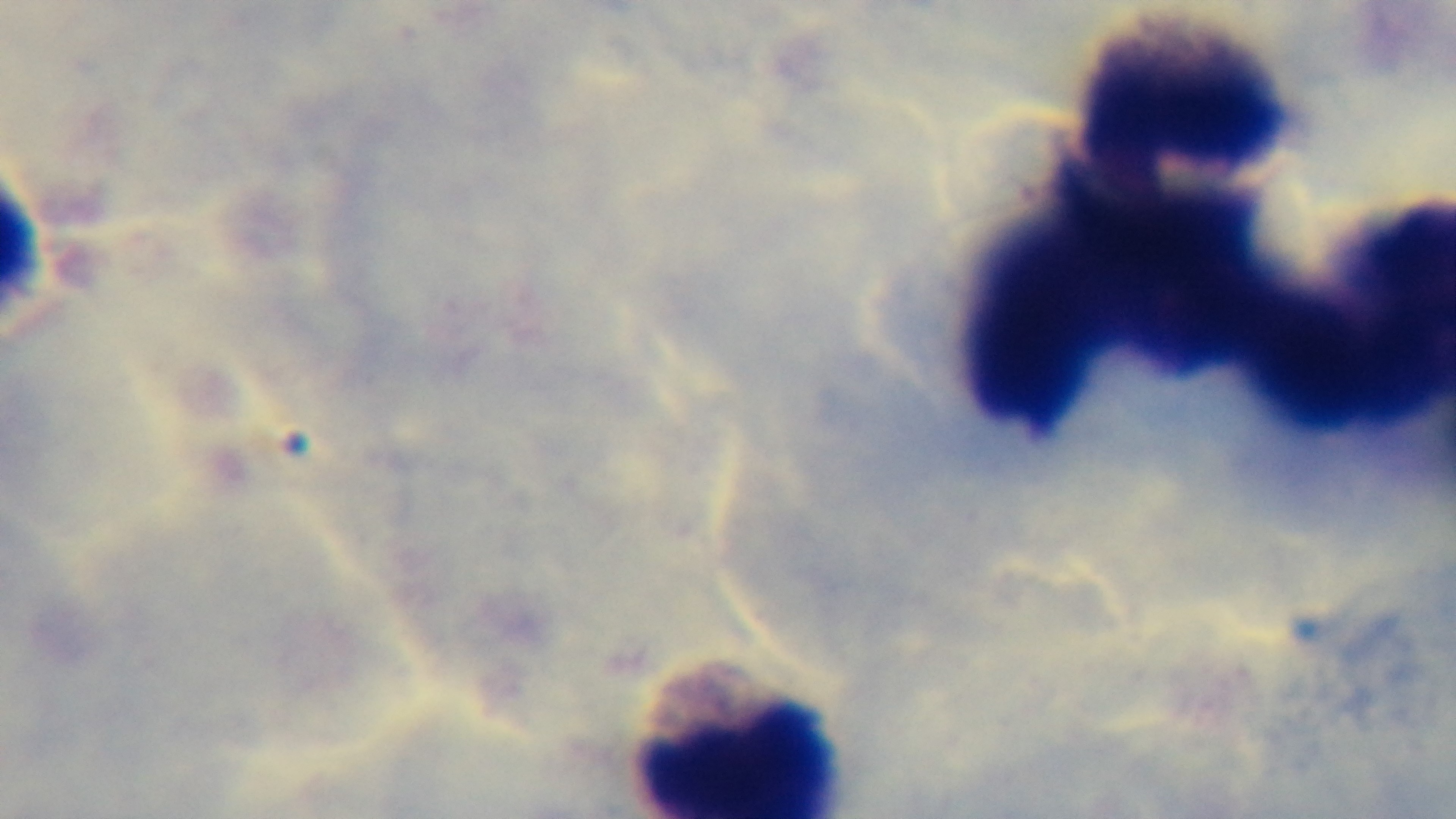

Preparation: thick smear. Malaria status: uninfected. Oil-immersion objective, 100x. One field from the slide. Photomicrograph. Giemsa-stained. Captured with a mounted 4K digital camera.